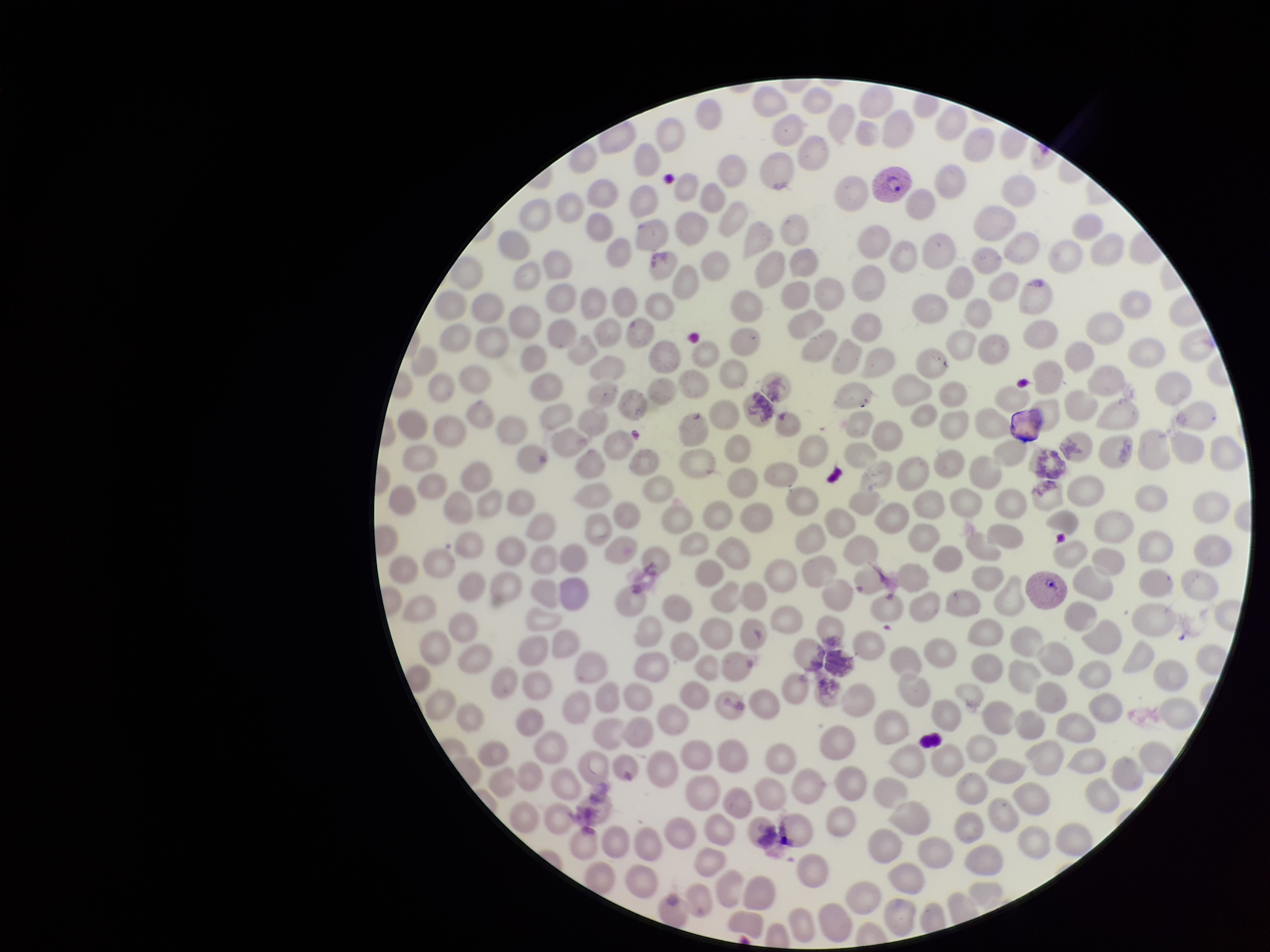

red_blood_cell_count: 262
parasitized_red_blood_cell_count: 2
species_reported_for_this_patient: Plasmodium vivax
image_size: 1270×952 pixels
field_of_view: single
parasitized_red_blood_cells: seen
capture: smartphone photograph through the microscope eyepiece
preparation: thin blood smear
stain: Giemsa
patient_malaria_status: infected